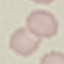
result = no malaria parasites detected
stain = Giemsa
preparation = thin blood smear
capture = smartphone through the microscope eyepiece
image type = automatically extracted cell patch, resized to 64 × 64 pixels